Identify the blood parasite species.
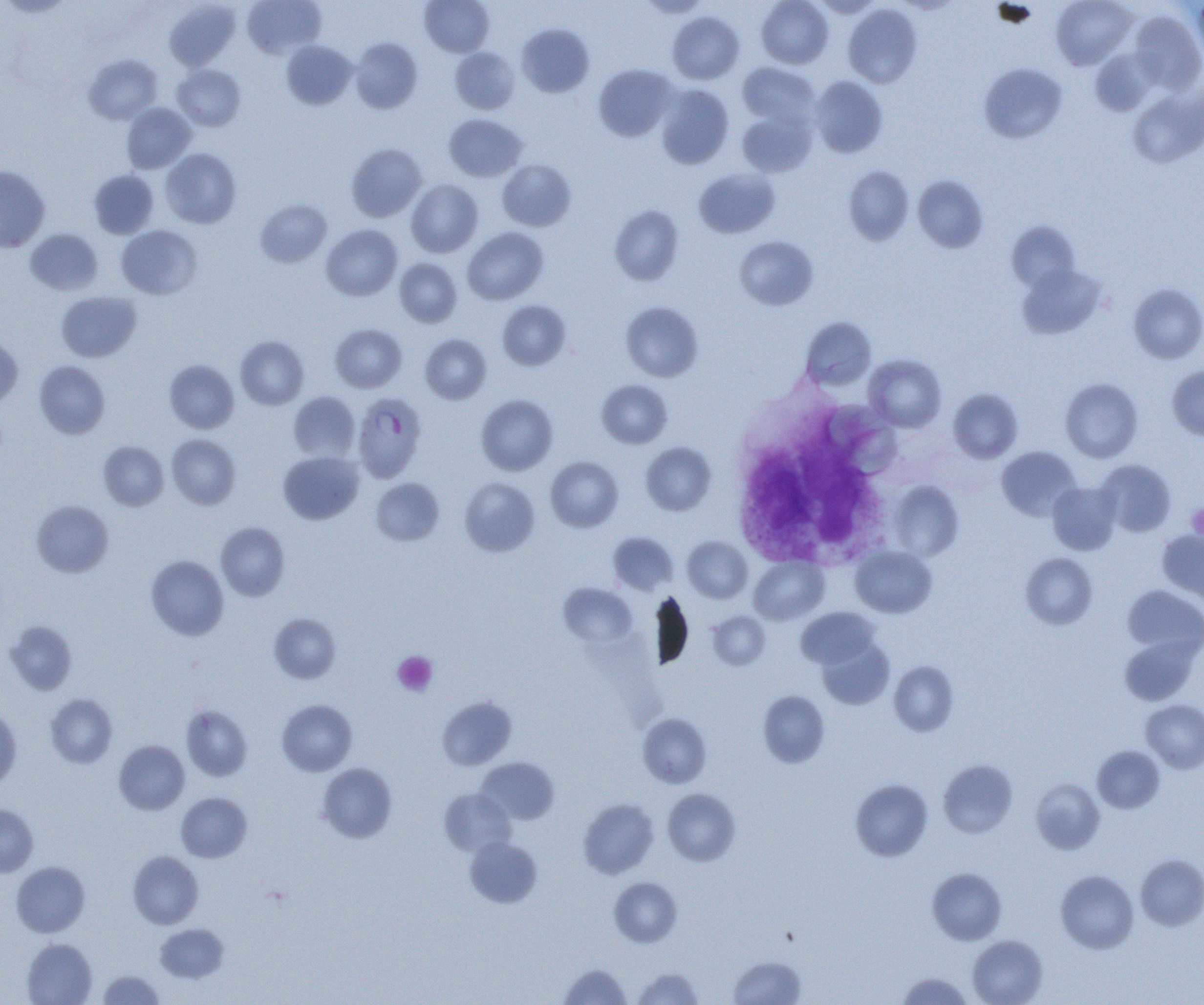
Plasmodium falciparum.

Approximate bounding boxes as (x1,y1)-(x2,y2) corner pairs in pixels. Plasmodium falciparum-infected red blood cell locations: (352,392)-(427,483). White blood cell locations: (730,409)-(895,573). Platelet locations: (1187,503)-(1204,538), (392,651)-(437,695). Uninfected red blood cell locations: (242,0)-(326,59), (420,0)-(494,57), (639,0)-(711,17), (756,0)-(833,68), (813,0)-(882,18), (1051,0)-(1136,69), (1192,0)-(1204,64), (0,1)-(75,18), (164,2)-(240,70), (842,4)-(922,88), (1129,10)-(1203,93), (667,11)-(744,84), (517,23)-(594,98), (350,38)-(422,114), (281,41)-(357,110), (450,47)-(519,114), (1089,48)-(1158,117), (83,54)-(162,124), (737,62)-(818,126), (979,63)-(1067,144), (172,64)-(246,131), (593,64)-(677,142), (810,76)-(888,158), (656,84)-(734,169), (1128,87)-(1204,168), (121,103)-(197,173), (737,110)-(816,177), (444,114)-(527,182), (346,143)-(427,222), (161,148)-(241,229), (497,159)-(576,231), (0,166)-(50,252), (843,166)-(914,245), (694,168)-(780,238), (89,169)-(159,238), (913,175)-(988,253), (406,180)-(483,257), (255,198)-(332,268), (609,204)-(684,286), (1005,220)-(1081,293), (321,224)-(402,301), (116,225)-(202,300), (462,227)-(547,305), (25,228)-(103,295), (734,235)-(818,310), (394,258)-(462,327), (1017,264)-(1107,339), (1128,284)-(1204,364), (56,291)-(142,362), (497,300)-(571,370), (620,301)-(703,382), (800,317)-(876,391), (329,323)-(407,392), (0,334)-(23,407), (420,334)-(492,404), (235,335)-(309,409), (863,354)-(947,432), (164,360)-(239,433), (34,361)-(110,439), (1167,366)-(1204,439), (1060,378)-(1144,462), (597,380)-(672,448), (948,389)-(1023,463), (288,392)-(360,462), (476,394)-(558,475), (167,434)-(241,509), (99,441)-(169,511), (640,442)-(716,516), (996,446)-(1080,520), (278,451)-(364,524), (545,456)-(623,532), (1096,459)-(1176,537), (459,477)-(540,557), (371,478)-(445,545), (888,481)-(964,561), (1047,482)-(1121,555), (31,499)-(114,578), (215,522)-(290,601), (1157,529)-(1204,600), (607,531)-(678,596), (682,536)-(753,603), (850,545)-(937,618), (1020,553)-(1098,630), (146,555)-(229,640), (749,556)-(829,625), (558,583)-(637,649), (1122,585)-(1204,660), (652,591)-(693,670), (796,607)-(880,670), (706,611)-(771,670), (269,613)-(340,684), (4,620)-(78,695), (1120,636)-(1199,705), (816,637)-(894,710), (889,661)-(959,736), (757,690)-(830,768), (45,694)-(118,768), (437,696)-(517,770), (277,699)-(357,776), (1141,699)-(1204,773), (181,705)-(253,781), (0,707)-(22,790), (638,713)-(712,788), (114,740)-(189,814), (1092,746)-(1164,813), (476,757)-(560,825), (937,759)-(1017,838), (317,763)-(397,843), (1031,778)-(1105,854), (850,779)-(933,861), (439,788)-(516,857), (662,789)-(741,866), (176,792)-(252,862), (578,798)-(658,879), (0,803)-(38,877), (465,836)-(542,907), (128,851)-(204,929), (1135,854)-(1204,931), (11,861)-(90,937), (927,867)-(1007,944), (1055,870)-(1139,954), (609,876)-(682,947), (155,923)-(229,982), (968,935)-(1047,1005), (22,938)-(97,1005), (728,955)-(806,1004), (559,963)-(632,1005), (631,966)-(704,1005), (97,970)-(165,1004), (896,972)-(972,1005). Image is 1204×1005 pixels. Thin blood smear. Light microscopy. Captured at 1000x magnification. Single field of view.